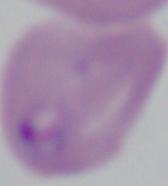
Photomicrograph. A Babesia parasite is seen. 1000x magnification.